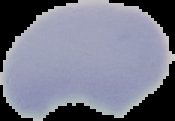
Summary:
  - Result: no malaria parasites seen
  - Image size: 175×121 pixels
  - Preparation: thin blood smear
  - Image type: segmented cell region with the area outside set to black